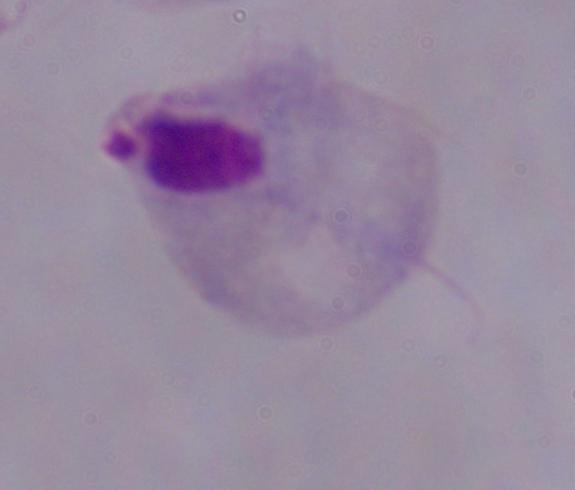

Summary:
  - Magnification: 1000x
  - Identification: trichomonad
  - Modality: micrograph